Point out each Plasmodium parasite.
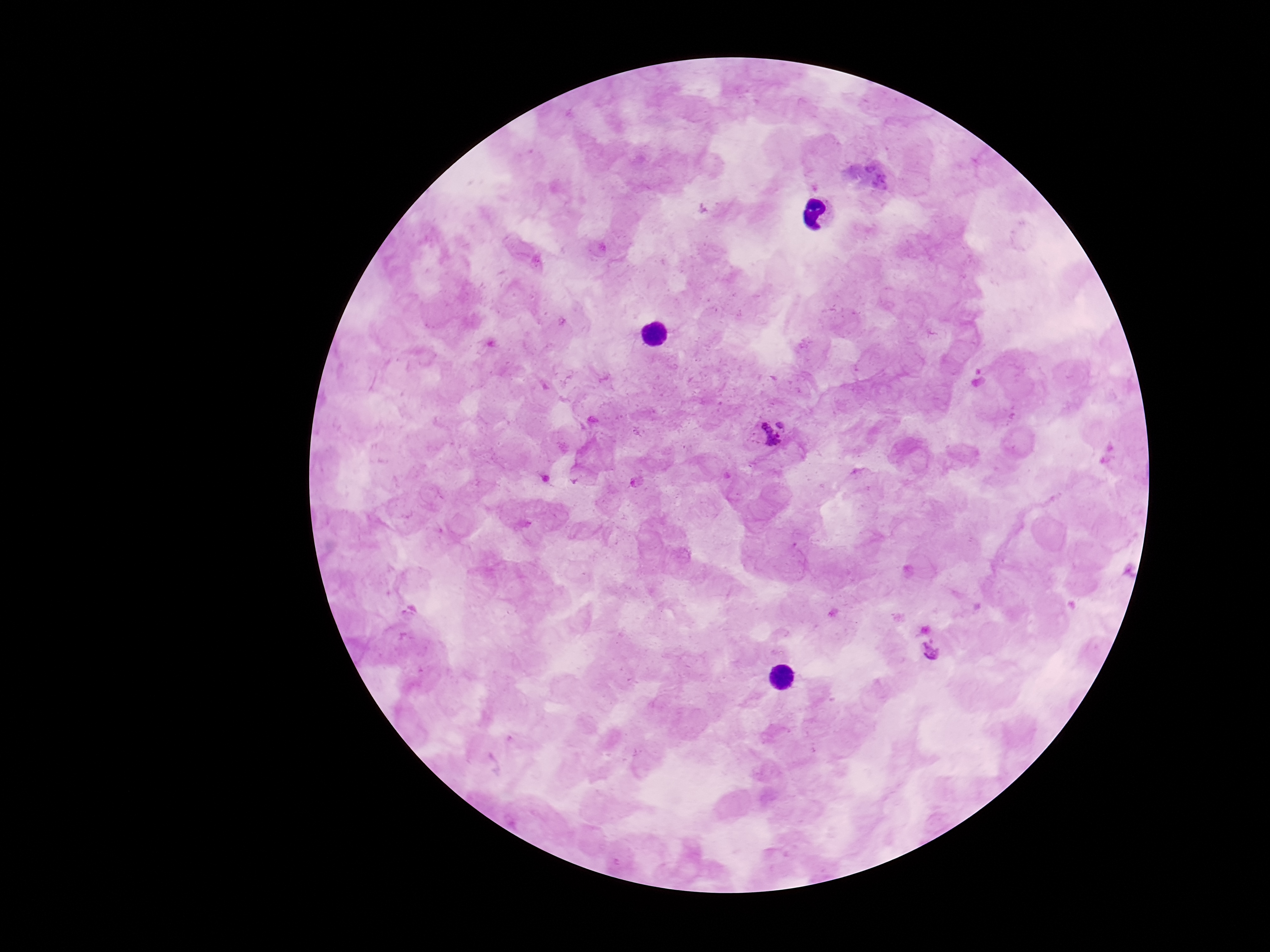

Approximate centers as {x, y} in pixels.
Plasmodium parasites: {771, 431}, {637, 482}, {932, 652}.

patient malaria status = positive
image size = 1270×952 pixels
stain = Giemsa
capture = smartphone camera through the microscope eyepiece
preparation = thick blood smear
field of view = single
magnification = 100x